Name the blood parasite species.
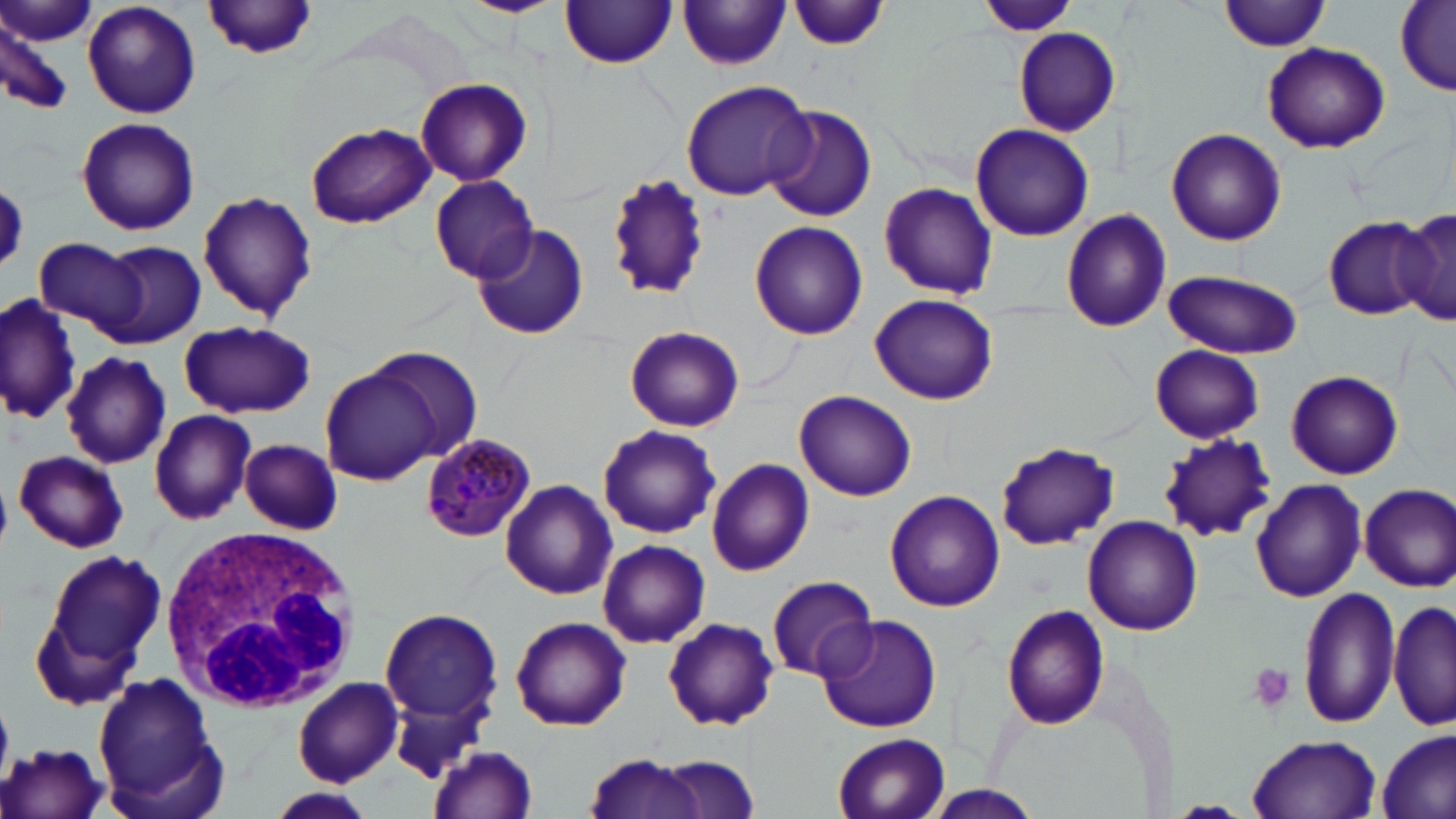
Plasmodium malariae.

Approximate bounding boxes as named x1/y1/x2/y2 corners in pixels. Platelet locations: (x1=1248, y1=662, x2=1298, y2=715). Plasmodium malariae-infected red blood cell locations: (x1=418, y1=434, x2=537, y2=543). Uninfected red blood cell locations: (x1=4, y1=0, x2=94, y2=48), (x1=82, y1=0, x2=201, y2=119), (x1=461, y1=0, x2=562, y2=17), (x1=978, y1=0, x2=1075, y2=38), (x1=1220, y1=0, x2=1334, y2=52), (x1=789, y1=1, x2=891, y2=51), (x1=561, y1=2, x2=679, y2=68), (x1=678, y1=2, x2=792, y2=71), (x1=203, y1=3, x2=322, y2=61), (x1=1397, y1=4, x2=1455, y2=94), (x1=0, y1=18, x2=72, y2=118), (x1=1012, y1=27, x2=1119, y2=136), (x1=1262, y1=42, x2=1389, y2=153), (x1=415, y1=76, x2=533, y2=185), (x1=680, y1=79, x2=812, y2=202), (x1=764, y1=104, x2=878, y2=222), (x1=76, y1=116, x2=201, y2=236), (x1=306, y1=123, x2=437, y2=229), (x1=970, y1=124, x2=1094, y2=241), (x1=1166, y1=127, x2=1286, y2=245), (x1=604, y1=174, x2=711, y2=300), (x1=429, y1=175, x2=539, y2=284), (x1=877, y1=179, x2=997, y2=301), (x1=197, y1=191, x2=318, y2=323), (x1=1394, y1=208, x2=1456, y2=327), (x1=1061, y1=210, x2=1172, y2=331), (x1=1322, y1=216, x2=1430, y2=319), (x1=750, y1=220, x2=867, y2=340), (x1=470, y1=222, x2=588, y2=343), (x1=33, y1=235, x2=146, y2=336), (x1=99, y1=240, x2=206, y2=348), (x1=1163, y1=268, x2=1303, y2=358), (x1=869, y1=292, x2=998, y2=405), (x1=2, y1=294, x2=82, y2=425), (x1=179, y1=320, x2=314, y2=418), (x1=624, y1=323, x2=745, y2=433), (x1=1149, y1=344, x2=1264, y2=444), (x1=361, y1=345, x2=487, y2=471), (x1=63, y1=351, x2=171, y2=470), (x1=321, y1=366, x2=442, y2=483), (x1=1286, y1=369, x2=1403, y2=479), (x1=795, y1=390, x2=916, y2=502), (x1=150, y1=410, x2=256, y2=525), (x1=597, y1=426, x2=722, y2=539), (x1=1158, y1=434, x2=1276, y2=543), (x1=238, y1=439, x2=345, y2=535), (x1=994, y1=440, x2=1120, y2=550), (x1=15, y1=450, x2=128, y2=553), (x1=705, y1=460, x2=814, y2=576), (x1=1250, y1=479, x2=1367, y2=602), (x1=499, y1=480, x2=617, y2=599), (x1=1359, y1=483, x2=1456, y2=592), (x1=884, y1=489, x2=1005, y2=612), (x1=1082, y1=516, x2=1203, y2=636), (x1=597, y1=538, x2=711, y2=649), (x1=41, y1=549, x2=167, y2=669), (x1=767, y1=575, x2=879, y2=681), (x1=1297, y1=586, x2=1402, y2=731), (x1=1389, y1=598, x2=1455, y2=732), (x1=1002, y1=605, x2=1112, y2=731), (x1=378, y1=608, x2=505, y2=729), (x1=816, y1=614, x2=941, y2=732), (x1=511, y1=615, x2=633, y2=732), (x1=662, y1=617, x2=779, y2=730), (x1=92, y1=673, x2=224, y2=814), (x1=292, y1=677, x2=405, y2=787), (x1=1375, y1=728, x2=1455, y2=819), (x1=832, y1=733, x2=952, y2=818), (x1=1249, y1=734, x2=1383, y2=818), (x1=0, y1=742, x2=112, y2=819), (x1=428, y1=744, x2=538, y2=819), (x1=581, y1=751, x2=705, y2=819), (x1=654, y1=755, x2=763, y2=819), (x1=923, y1=785, x2=1045, y2=818), (x1=271, y1=787, x2=375, y2=819). White blood cell locations: (x1=160, y1=524, x2=361, y2=713). Thin blood film. May-Grünwald-Giemsa-stained preparation. Single field of view. Optical microscopy. Captured at 1000x magnification. Image is 1456×819 pixels.